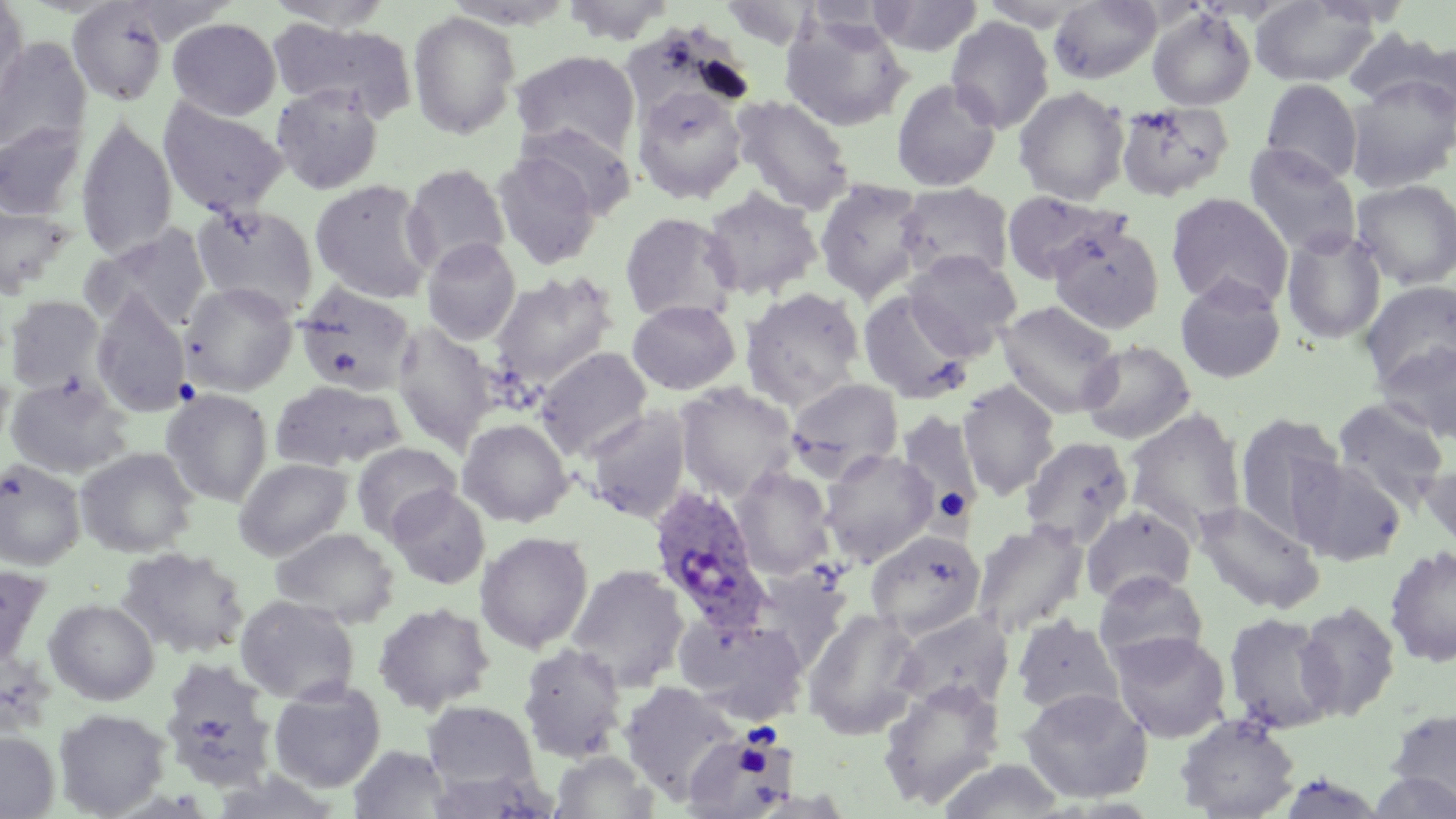
slide-level diagnosis = Plasmodium ovale
preparation = thin blood smear
stain = May-Grünwald-Giemsa
Plasmodium ovale-infected red blood cell locations = approximate bounding boxes as named x1/y1/x2/y2 corners in pixels: (x1=646, y1=483, x2=773, y2=632)
field of view = single
uninfected red blood cell locations = approximate bounding boxes as named x1/y1/x2/y2 corners in pixels: (x1=262, y1=0, x2=397, y2=31), (x1=561, y1=0, x2=676, y2=44), (x1=871, y1=0, x2=984, y2=57), (x1=68, y1=1, x2=170, y2=106), (x1=719, y1=1, x2=817, y2=49), (x1=977, y1=1, x2=1094, y2=30), (x1=1048, y1=1, x2=1163, y2=84), (x1=1250, y1=1, x2=1381, y2=88), (x1=0, y1=2, x2=28, y2=106), (x1=1147, y1=7, x2=1257, y2=111), (x1=407, y1=10, x2=521, y2=140), (x1=780, y1=14, x2=912, y2=132), (x1=946, y1=16, x2=1055, y2=134), (x1=167, y1=17, x2=282, y2=120), (x1=270, y1=19, x2=418, y2=122), (x1=1343, y1=28, x2=1456, y2=117), (x1=0, y1=37, x2=92, y2=158), (x1=511, y1=50, x2=641, y2=161), (x1=1345, y1=74, x2=1456, y2=192), (x1=891, y1=78, x2=1002, y2=191), (x1=1260, y1=79, x2=1363, y2=185), (x1=271, y1=84, x2=383, y2=195), (x1=631, y1=86, x2=749, y2=205), (x1=1013, y1=86, x2=1130, y2=204), (x1=731, y1=94, x2=855, y2=215), (x1=158, y1=97, x2=288, y2=218), (x1=1115, y1=101, x2=1234, y2=202), (x1=76, y1=118, x2=178, y2=262), (x1=518, y1=121, x2=637, y2=219), (x1=0, y1=123, x2=85, y2=220), (x1=1244, y1=143, x2=1362, y2=258), (x1=492, y1=150, x2=602, y2=272), (x1=402, y1=163, x2=511, y2=276), (x1=310, y1=179, x2=436, y2=303), (x1=814, y1=179, x2=925, y2=303), (x1=1351, y1=179, x2=1456, y2=290), (x1=895, y1=182, x2=1014, y2=283), (x1=701, y1=188, x2=822, y2=301), (x1=1002, y1=191, x2=1131, y2=286), (x1=1166, y1=193, x2=1293, y2=311), (x1=192, y1=203, x2=319, y2=318), (x1=0, y1=205, x2=73, y2=299), (x1=619, y1=212, x2=739, y2=323), (x1=1049, y1=221, x2=1164, y2=335), (x1=87, y1=224, x2=212, y2=332), (x1=1281, y1=227, x2=1387, y2=345), (x1=422, y1=238, x2=521, y2=345), (x1=904, y1=250, x2=1022, y2=358), (x1=489, y1=271, x2=618, y2=390), (x1=1174, y1=275, x2=1287, y2=384), (x1=1360, y1=280, x2=1456, y2=390), (x1=180, y1=282, x2=299, y2=395), (x1=294, y1=282, x2=417, y2=396), (x1=740, y1=287, x2=866, y2=408), (x1=857, y1=289, x2=974, y2=404), (x1=91, y1=293, x2=191, y2=416), (x1=4, y1=295, x2=106, y2=394), (x1=627, y1=299, x2=741, y2=395), (x1=996, y1=299, x2=1122, y2=418), (x1=392, y1=323, x2=498, y2=451), (x1=1078, y1=339, x2=1195, y2=444), (x1=1375, y1=341, x2=1456, y2=444), (x1=535, y1=346, x2=653, y2=460), (x1=4, y1=375, x2=132, y2=479), (x1=787, y1=377, x2=903, y2=478), (x1=957, y1=379, x2=1061, y2=500), (x1=272, y1=380, x2=405, y2=472), (x1=675, y1=382, x2=798, y2=500), (x1=161, y1=388, x2=273, y2=506), (x1=1331, y1=397, x2=1451, y2=509), (x1=583, y1=406, x2=692, y2=524), (x1=1124, y1=408, x2=1247, y2=538), (x1=896, y1=411, x2=984, y2=518), (x1=1235, y1=413, x2=1346, y2=542), (x1=457, y1=418, x2=573, y2=527), (x1=1020, y1=436, x2=1134, y2=547), (x1=352, y1=442, x2=461, y2=541), (x1=75, y1=447, x2=198, y2=558), (x1=820, y1=448, x2=938, y2=565), (x1=233, y1=457, x2=353, y2=560), (x1=1294, y1=458, x2=1407, y2=566), (x1=0, y1=460, x2=85, y2=570), (x1=1420, y1=460, x2=1456, y2=551), (x1=732, y1=466, x2=835, y2=579), (x1=386, y1=486, x2=491, y2=589), (x1=1193, y1=501, x2=1325, y2=614), (x1=1081, y1=506, x2=1196, y2=605), (x1=971, y1=520, x2=1089, y2=637), (x1=270, y1=527, x2=399, y2=627), (x1=865, y1=529, x2=986, y2=639), (x1=475, y1=531, x2=594, y2=653), (x1=115, y1=546, x2=250, y2=659), (x1=1384, y1=546, x2=1456, y2=667), (x1=0, y1=563, x2=52, y2=673), (x1=567, y1=564, x2=690, y2=691), (x1=749, y1=569, x2=850, y2=671), (x1=1093, y1=571, x2=1208, y2=670), (x1=235, y1=595, x2=360, y2=705), (x1=44, y1=598, x2=159, y2=705), (x1=1295, y1=601, x2=1401, y2=721), (x1=373, y1=602, x2=495, y2=714), (x1=802, y1=608, x2=924, y2=741), (x1=893, y1=611, x2=1014, y2=714), (x1=1223, y1=612, x2=1340, y2=734), (x1=677, y1=614, x2=808, y2=723), (x1=1011, y1=614, x2=1123, y2=717), (x1=1110, y1=630, x2=1232, y2=743), (x1=517, y1=643, x2=628, y2=763), (x1=164, y1=655, x2=284, y2=789), (x1=877, y1=678, x2=1006, y2=809), (x1=269, y1=681, x2=386, y2=793), (x1=619, y1=681, x2=742, y2=801), (x1=1019, y1=687, x2=1154, y2=804), (x1=422, y1=700, x2=541, y2=796), (x1=54, y1=708, x2=171, y2=818), (x1=1386, y1=708, x2=1455, y2=809), (x1=1174, y1=713, x2=1300, y2=819), (x1=682, y1=729, x2=795, y2=818), (x1=0, y1=731, x2=59, y2=818), (x1=349, y1=745, x2=451, y2=818), (x1=550, y1=750, x2=658, y2=818), (x1=938, y1=759, x2=1066, y2=818), (x1=425, y1=767, x2=560, y2=818), (x1=1273, y1=771, x2=1390, y2=818), (x1=1365, y1=772, x2=1455, y2=818)
image size = 1456×819 pixels
magnification = 1000x
modality = light microscopy